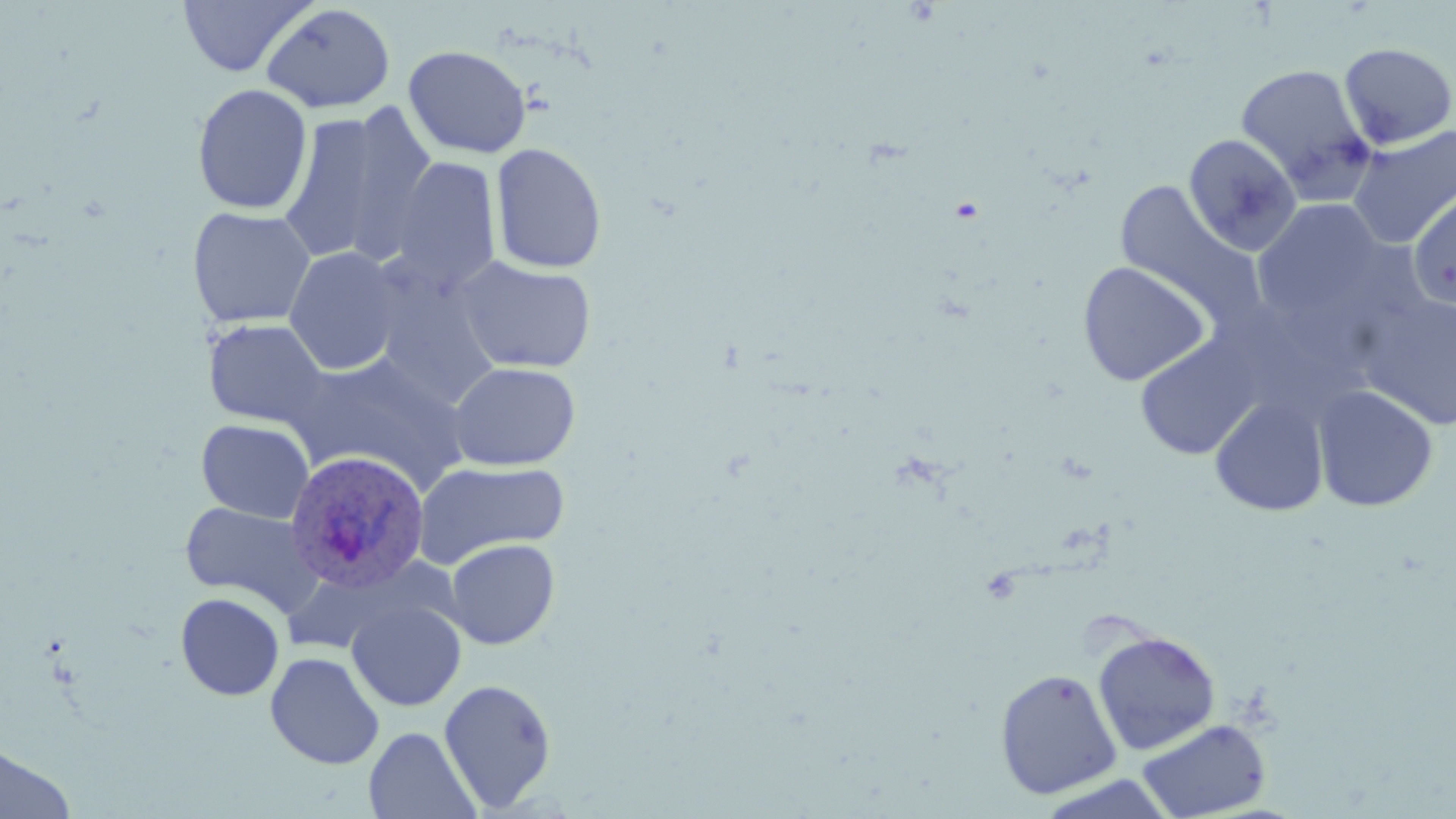
Approximate bounding boxes as (x1,y1)-(x2,y2) corner pairs in pixels. Uninfected red blood cell locations: (177,0)-(314,77), (261,4)-(395,113), (1338,42)-(1456,150), (401,43)-(523,283), (403,45)-(532,158), (1235,63)-(1377,201), (192,83)-(313,215), (277,106)-(435,267), (1348,125)-(1456,248), (1183,134)-(1301,256), (490,142)-(607,274), (390,157)-(501,296), (1113,181)-(1267,336), (1407,188)-(1456,311), (1253,198)-(1388,326), (187,206)-(317,328), (283,246)-(403,376), (454,256)-(597,374), (1077,260)-(1212,386), (1360,293)-(1456,430), (203,319)-(329,429), (1134,335)-(1264,460), (285,353)-(472,492), (447,361)-(581,471), (1313,384)-(1439,512), (1208,395)-(1329,517), (196,418)-(314,523), (414,460)-(571,568), (180,501)-(322,613), (444,538)-(560,649), (175,592)-(285,701), (346,598)-(467,712), (1091,629)-(1221,755), (265,652)-(384,770), (994,667)-(1122,799), (438,678)-(557,813), (1137,718)-(1271,818), (363,727)-(481,819), (0,741)-(77,819). Plasmodium ovale-infected red blood cell locations: (284,449)-(432,595). Slide-level diagnosis: Plasmodium ovale. Thin blood smear. Image is 1456×819 pixels. One field of a larger specimen. Captured at 1000x magnification. May-Grünwald-Giemsa stain. Optical microscopy.